Identify the parasite.
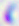

This is Toxoplasma gondii.

Summary:
  - Magnification: 400x
  - Modality: micrograph